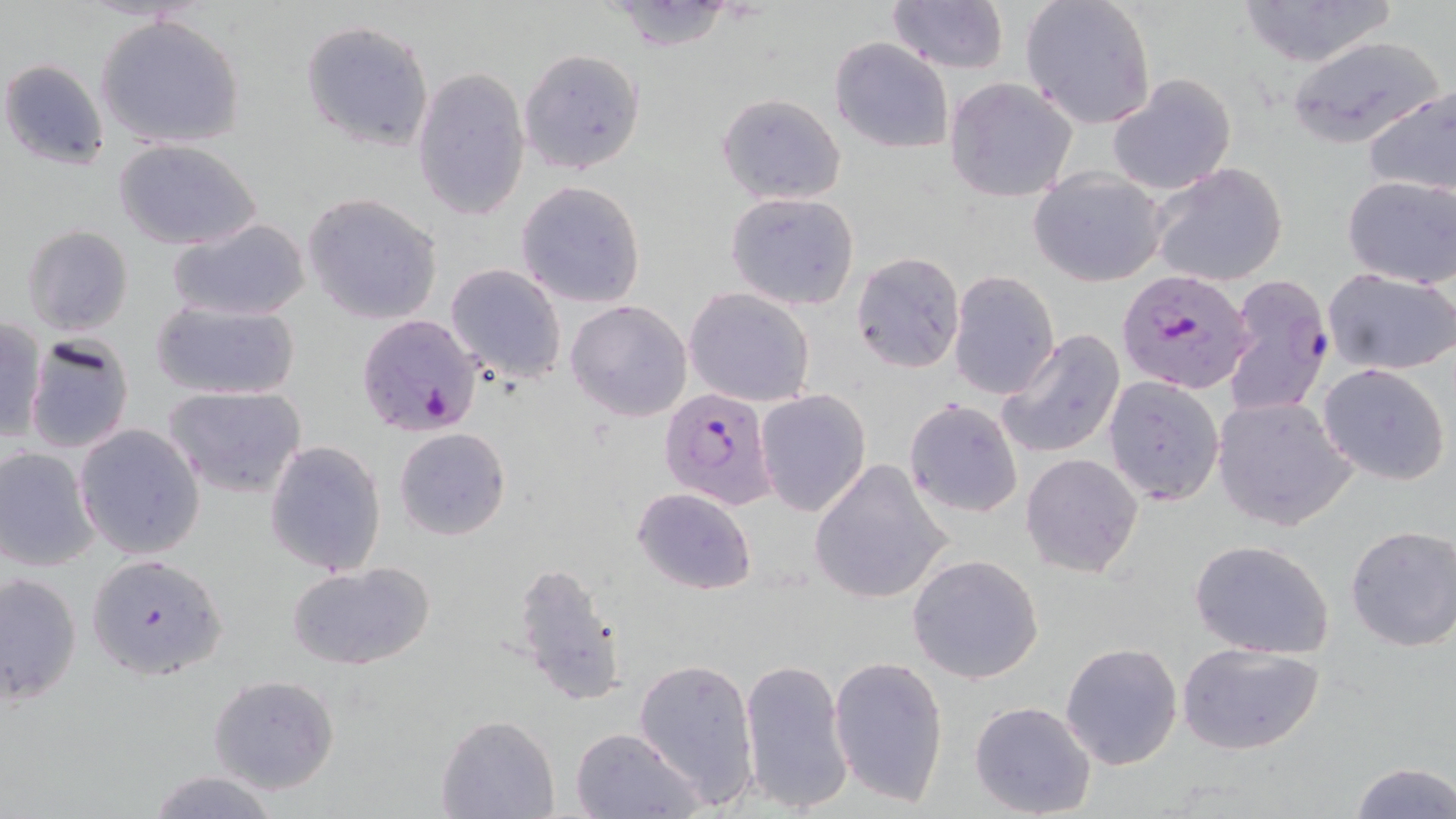
slide-level diagnosis = Plasmodium falciparum
image size = 1456×819 pixels
Plasmodium falciparum-infected red blood cell locations = approximate bounding boxes as (x1, y1, x2, y2) in pixels: (1118, 269, 1256, 395), (1222, 272, 1335, 421), (356, 316, 485, 438), (659, 388, 779, 508)
field of view = single
uninfected red blood cell locations = approximate bounding boxes as (x1, y1, x2, y2) in pixels: (887, 0, 1009, 73), (1020, 0, 1158, 130), (1236, 0, 1396, 68), (602, 1, 738, 51), (95, 13, 247, 151), (300, 19, 435, 152), (1286, 36, 1444, 148), (830, 37, 954, 155), (519, 49, 645, 175), (0, 58, 111, 172), (411, 66, 529, 224), (1107, 73, 1236, 194), (944, 77, 1078, 203), (1362, 84, 1456, 200), (716, 92, 847, 205), (113, 137, 263, 251), (1150, 163, 1289, 287), (1028, 168, 1168, 287), (1342, 175, 1456, 287), (515, 181, 646, 309), (724, 191, 860, 312), (302, 193, 444, 324), (168, 218, 312, 321), (23, 225, 134, 337), (850, 250, 965, 373), (444, 263, 568, 383), (1323, 266, 1456, 378), (948, 271, 1061, 399), (684, 287, 816, 407), (149, 298, 303, 401), (565, 299, 693, 422), (0, 316, 47, 443), (997, 328, 1126, 461), (24, 334, 134, 454), (1318, 363, 1451, 486), (1101, 375, 1226, 506), (163, 386, 308, 500), (755, 388, 871, 517), (1212, 396, 1355, 531), (903, 398, 1023, 520), (74, 423, 205, 561), (393, 426, 511, 540), (263, 438, 385, 578), (0, 445, 100, 571), (1021, 452, 1143, 578), (808, 458, 953, 605), (632, 486, 756, 596), (1344, 526, 1456, 651), (1189, 539, 1336, 659), (85, 554, 229, 680), (907, 554, 1045, 684), (287, 561, 435, 671), (511, 561, 627, 708), (0, 571, 82, 707), (1175, 641, 1326, 755), (1060, 642, 1183, 769), (829, 653, 948, 809), (633, 656, 760, 806), (739, 656, 852, 813), (208, 674, 340, 795), (969, 700, 1097, 818), (436, 715, 561, 819), (570, 727, 704, 818), (1345, 760, 1455, 818), (144, 770, 282, 819)
magnification = 1000x
modality = light microscopy
preparation = thin blood smear
stain = May-Grünwald-Giemsa